Classify this cell by malaria status.
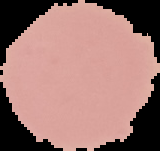

It is uninfected.

Summary:
  - Image size: 160×151 pixels
  - Preparation: thin blood film
  - Image type: cell region segmented out of the field of view; surrounding area masked to black